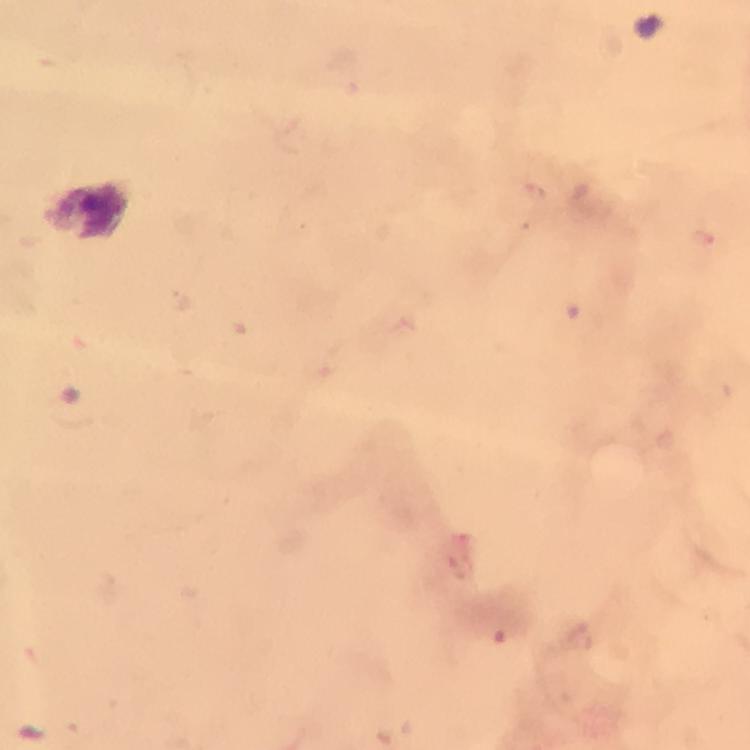
Approximate centers as {x, y} in pixels. Malaria parasite locations: {534, 192}, {705, 238}, {461, 567}, {498, 637}. From a malaria diagnostic workup. Immersion oil was used. Smartphone photograph taken through a microscope. Giemsa-stained preparation. Image is 750×750 pixels. 100x magnification. A crop from one field of view. Thick blood smear.